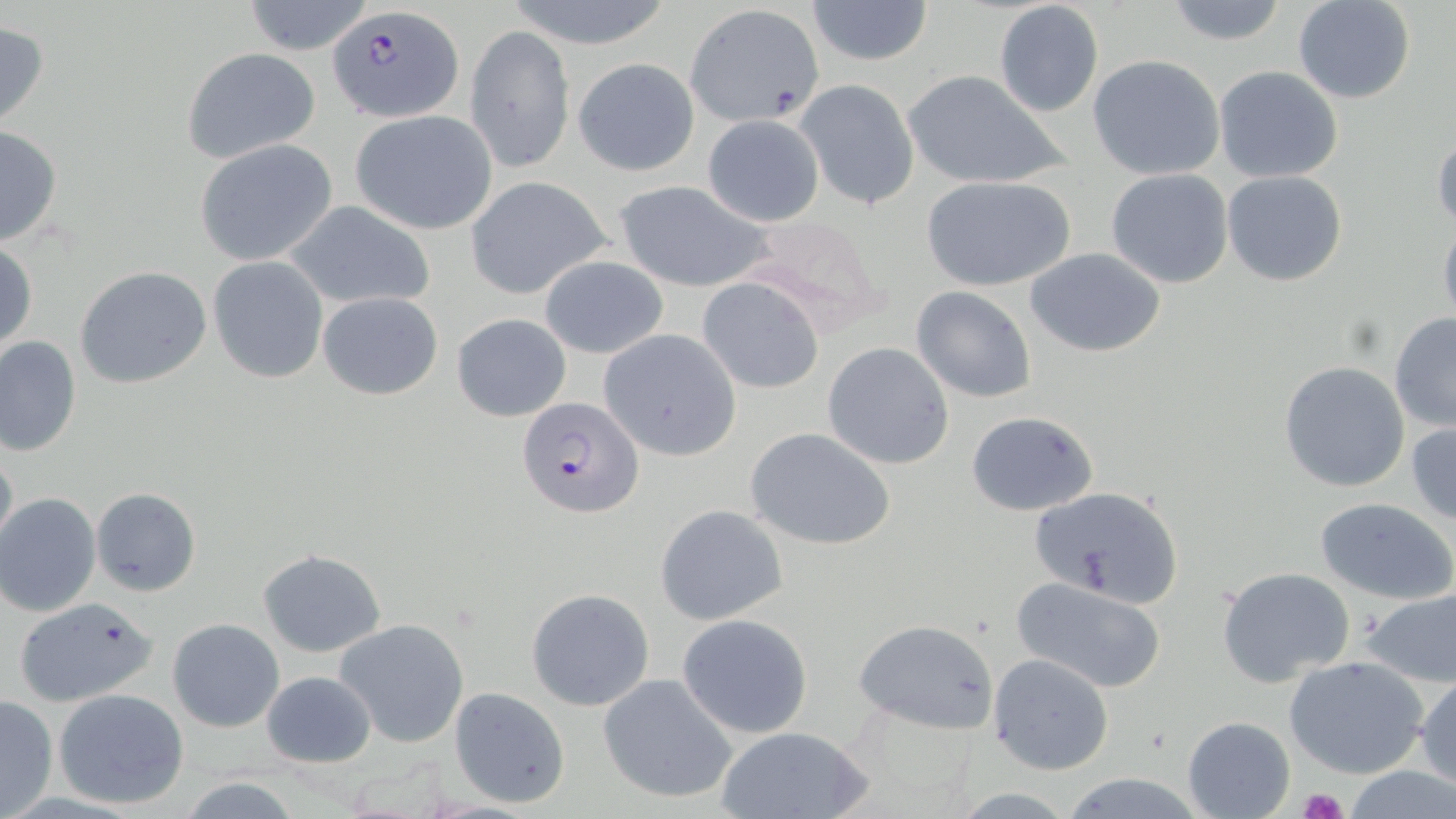
plasmodium_falciparum_infected_red_blood_cell_locations: 'approximate bounding boxes as [x1, y1, x2, y2] in pixels: [324, 6, 465, 124], [517, 397, 643, 519]'
slide_level_diagnosis: Plasmodium falciparum
platelet_locations: 'approximate bounding boxes as [x1, y1, x2, y2] in pixels: [1301, 789, 1347, 819]'
preparation: thin blood film
modality: light microscopy
stain: May-Grünwald-Giemsa
magnification: 1000x
field_of_view: single
uninfected_red_blood_cell_locations: 'approximate bounding boxes as [x1, y1, x2, y2] in pixels: [242, 0, 376, 55], [502, 0, 679, 50], [804, 0, 934, 66], [1293, 0, 1417, 104], [993, 1, 1105, 117], [1159, 2, 1295, 47], [686, 3, 824, 127], [0, 19, 50, 131], [466, 24, 574, 174], [179, 47, 322, 165], [1087, 54, 1226, 179], [573, 57, 699, 176], [1212, 66, 1346, 184], [901, 69, 1070, 191], [796, 78, 921, 212], [351, 110, 499, 235], [702, 113, 825, 227], [0, 123, 63, 247], [1431, 129, 1455, 232], [193, 139, 337, 266], [1104, 168, 1234, 289], [1222, 171, 1348, 287], [919, 175, 1076, 293], [465, 176, 613, 301], [611, 181, 776, 293], [281, 198, 437, 311], [734, 214, 887, 335], [1438, 217, 1456, 331], [0, 239, 37, 358], [1025, 246, 1167, 358], [539, 255, 668, 359], [207, 257, 328, 382], [75, 267, 213, 390], [695, 276, 825, 395], [911, 285, 1038, 404], [317, 291, 443, 400], [1389, 311, 1456, 432], [452, 312, 571, 421], [598, 330, 741, 460], [0, 335, 81, 456], [821, 343, 954, 470], [1278, 361, 1410, 493], [965, 410, 1100, 517], [1406, 419, 1456, 524], [745, 427, 896, 552], [0, 445, 16, 556], [1028, 484, 1184, 605], [91, 488, 201, 596], [1, 493, 101, 616], [1315, 497, 1456, 603], [655, 504, 787, 625], [256, 548, 386, 656], [1216, 566, 1356, 686], [1012, 575, 1169, 693], [1357, 586, 1456, 689], [525, 589, 655, 711], [12, 596, 162, 708], [677, 612, 814, 739], [168, 618, 283, 732], [334, 618, 470, 748], [853, 618, 1000, 736], [988, 653, 1114, 775], [1283, 654, 1429, 779], [261, 670, 375, 769], [1414, 671, 1456, 790], [597, 673, 739, 804], [447, 686, 571, 809], [53, 688, 189, 810], [1, 694, 58, 818], [1182, 716, 1294, 819], [714, 725, 871, 819], [1342, 766, 1456, 818], [1056, 772, 1214, 818], [175, 777, 306, 817]'
image_size: 1456×819 pixels